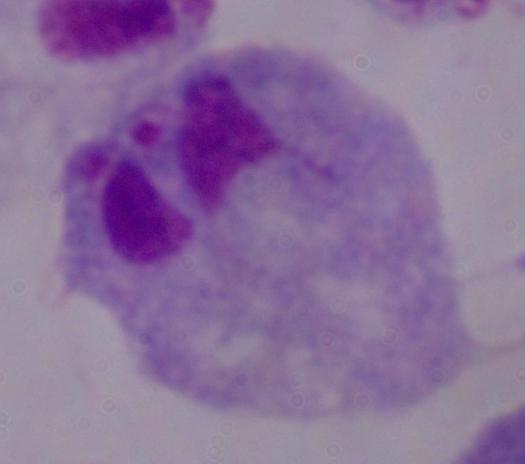 Captured at 1000x magnification. A trichomonad is shown. Photomicrograph.